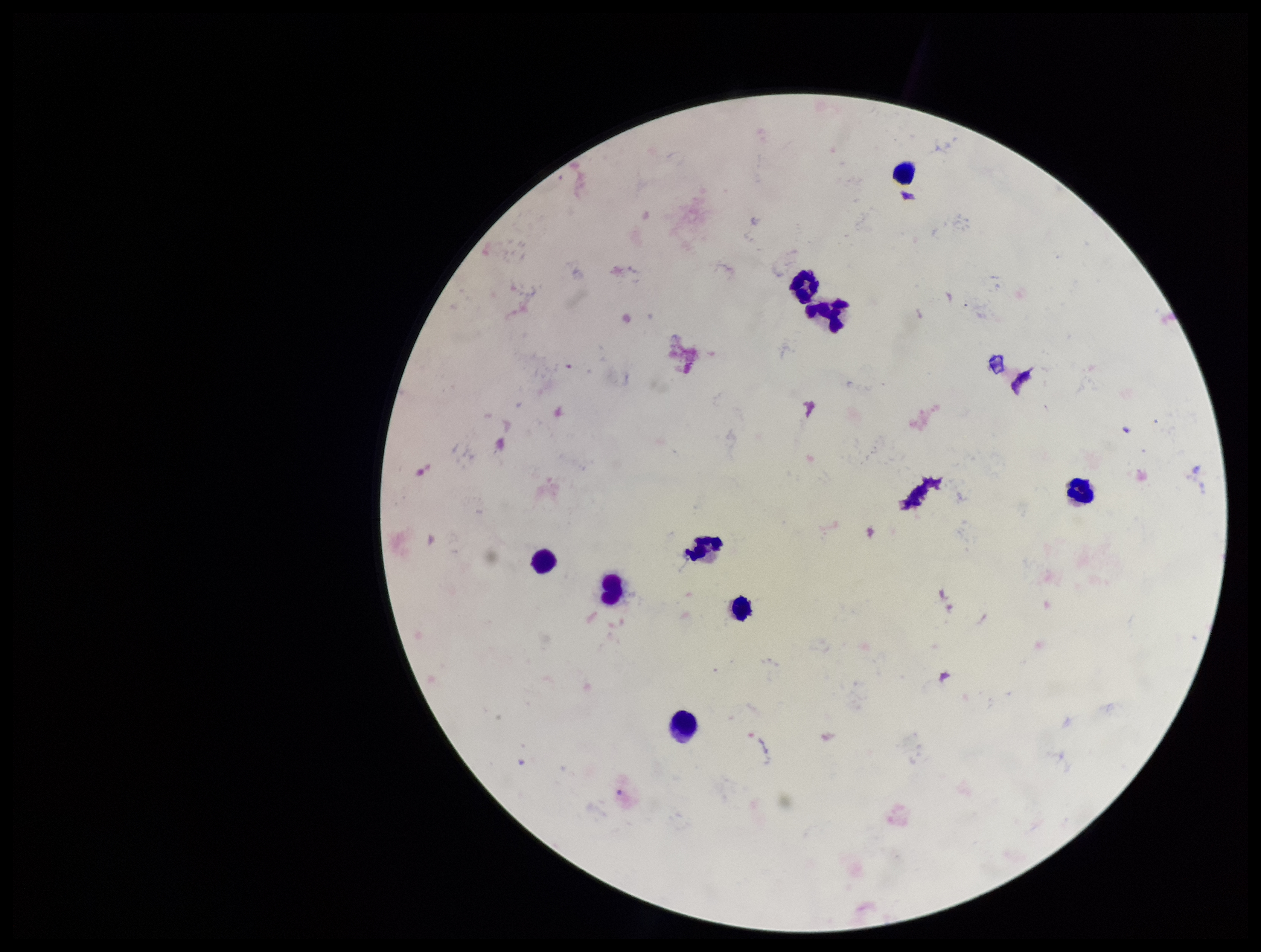
Summary:
  - Preparation: thick smear
  - Parasite count: 0
  - Capture: smartphone photograph through the microscope eyepiece
  - Field of view: one from this slide
  - Patient malaria status: negative
  - Stain: Giemsa
  - Plasmodium parasites: none detected
  - Image size: 1261×952 pixels
  - Leukocyte count: 9